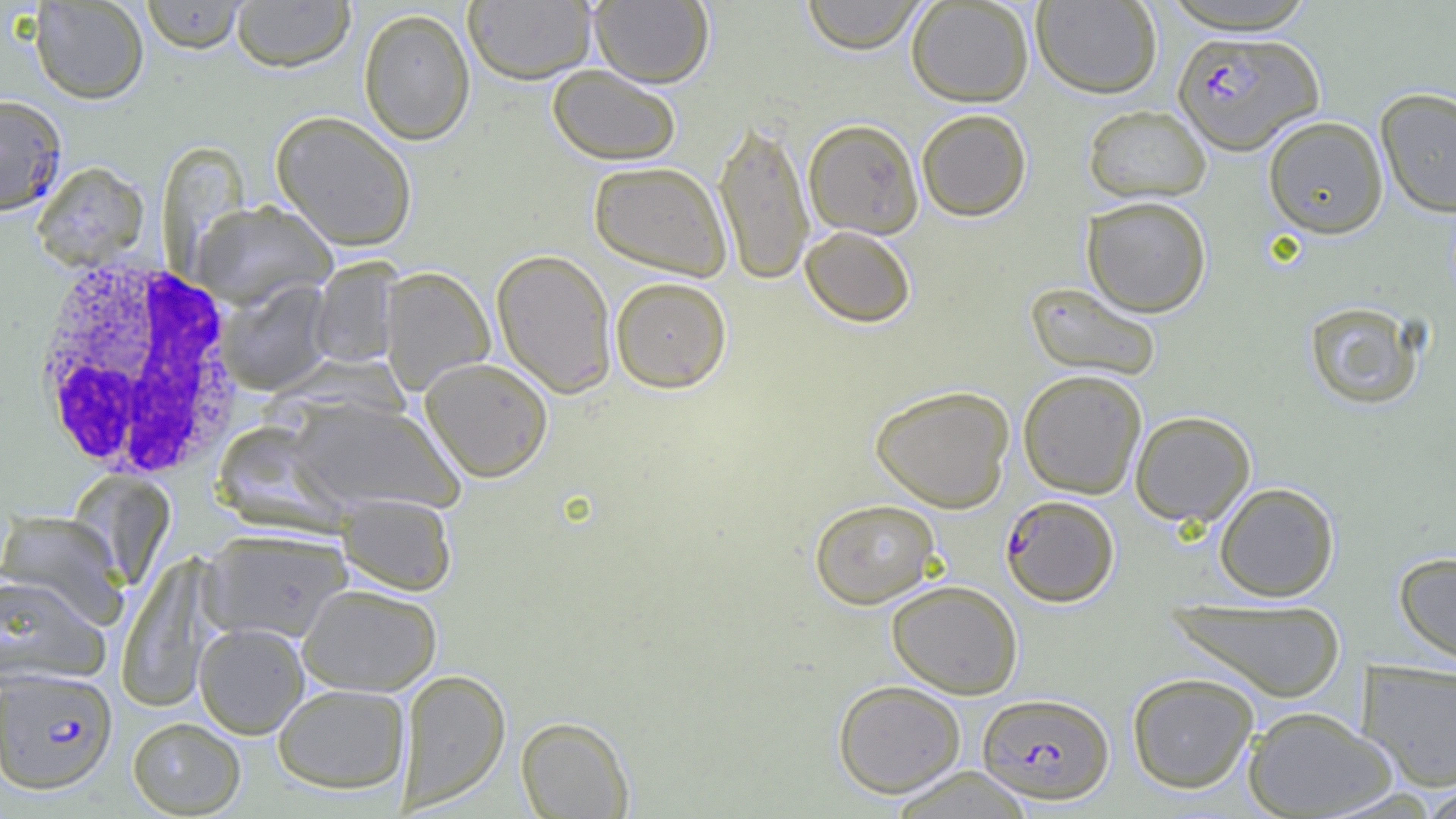
slide-level diagnosis = Plasmodium falciparum
uninfected red blood cell locations = approximate bounding boxes as [x1, y1, x2, y2] in pixels: [29, 0, 149, 104], [140, 0, 249, 54], [230, 0, 356, 72], [463, 0, 596, 84], [589, 0, 714, 87], [800, 0, 929, 54], [906, 0, 1034, 106], [1031, 0, 1162, 98], [1159, 1, 1320, 34], [358, 8, 476, 145], [547, 64, 682, 165], [1375, 88, 1456, 218], [1083, 104, 1212, 203], [916, 108, 1032, 221], [271, 110, 418, 251], [1263, 115, 1388, 238], [713, 116, 815, 285], [803, 118, 924, 239], [158, 142, 250, 265], [588, 160, 733, 280], [31, 162, 150, 270], [1082, 195, 1212, 317], [191, 201, 337, 309], [800, 225, 916, 328], [492, 248, 617, 397], [309, 258, 402, 369], [379, 267, 495, 395], [610, 276, 732, 393], [218, 281, 333, 395], [1024, 282, 1163, 382], [1303, 300, 1425, 410], [420, 357, 553, 482], [1017, 369, 1148, 499], [869, 384, 1015, 512], [288, 398, 464, 515], [1129, 410, 1256, 526], [68, 471, 176, 590], [1214, 482, 1339, 601], [336, 493, 457, 596], [809, 498, 940, 608], [0, 510, 129, 629], [200, 529, 353, 643], [1394, 550, 1456, 668], [116, 556, 219, 712], [0, 574, 110, 687], [886, 579, 1024, 699], [298, 583, 443, 696], [1166, 598, 1347, 702], [194, 622, 309, 739], [1357, 660, 1456, 791], [396, 668, 510, 811], [1127, 672, 1259, 793], [833, 679, 966, 798], [273, 684, 410, 794], [1242, 706, 1398, 818], [516, 716, 634, 818], [127, 717, 246, 817], [886, 767, 1036, 819]
image size = 1456×819 pixels
preparation = thin blood film
modality = light microscopy
field of view = one of a larger specimen
white blood cell locations = approximate bounding boxes as [x1, y1, x2, y2] in pixels: [26, 254, 249, 482]
Plasmodium falciparum-infected red blood cell locations = approximate bounding boxes as [x1, y1, x2, y2] in pixels: [1173, 30, 1323, 155], [0, 94, 67, 216], [1001, 494, 1119, 606], [0, 668, 118, 795], [977, 692, 1114, 803]
magnification = 1000x